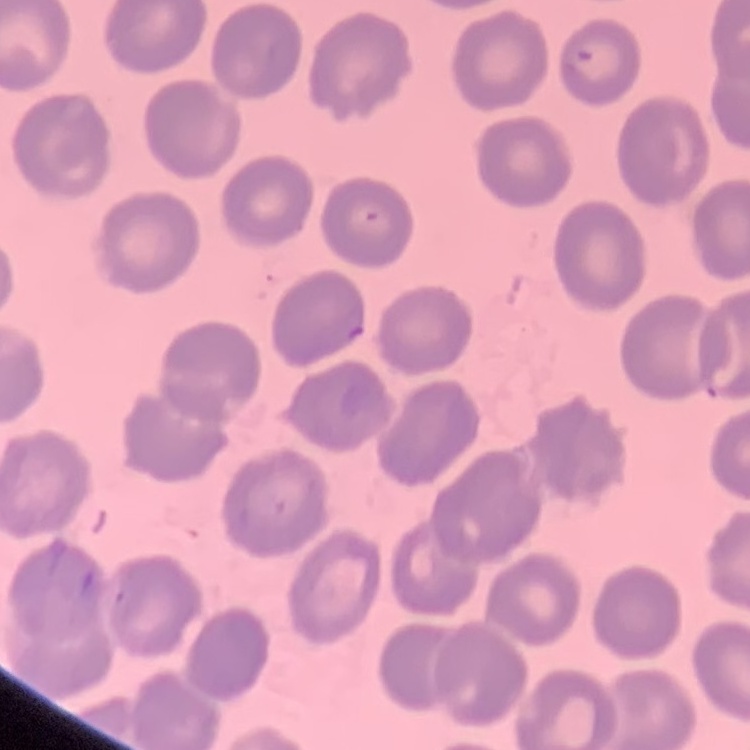

The erythrocytes show no rouleaux formation. Stained with either Field's or Giemsa. Square crop of a larger photomicrograph. Thin peripheral smear.